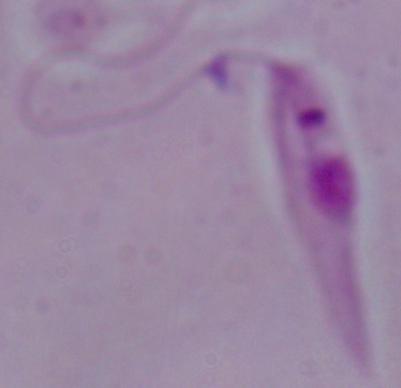 A Leishmania parasite is seen. Captured at 1000x magnification. Photomicrograph.